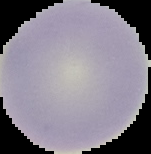 Result: no Plasmodium parasites seen. From a thin blood smear. Image is 151×154 pixels. Cell region segmented out of the field of view; the surrounding area is masked to black.